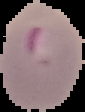
{
  "image_size": "85×112 pixels",
  "preparation": "thin blood smear",
  "image_type": "cell region segmented out of the field of view; surrounding area masked to black",
  "malaria_status": "parasitized"
}